Describe the morphology of the erythrocytes.
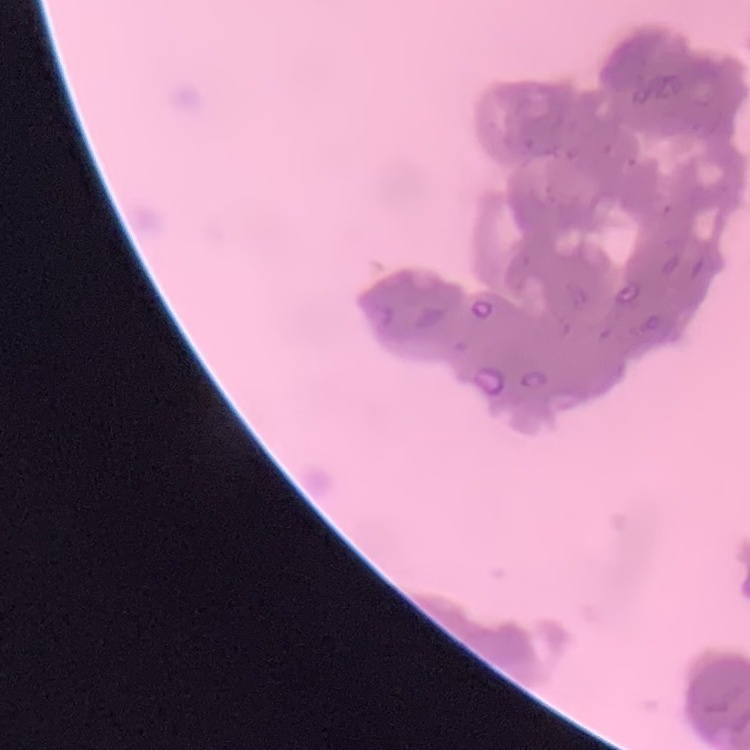
They show rouleaux formation.

{
  "image_type": "one tile cut from a larger photomicrograph",
  "stain": "Field's or Giemsa",
  "preparation": "thin blood film"
}